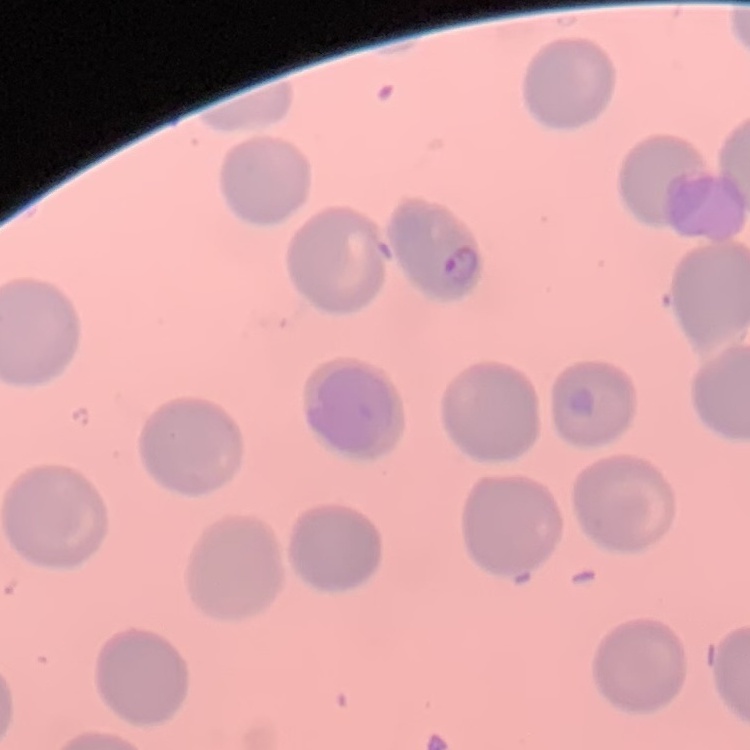
red blood cell morphology = no rouleaux formation
preparation = thin blood smear
image type = one tile cut from a larger photomicrograph
stain = Field's or Giemsa